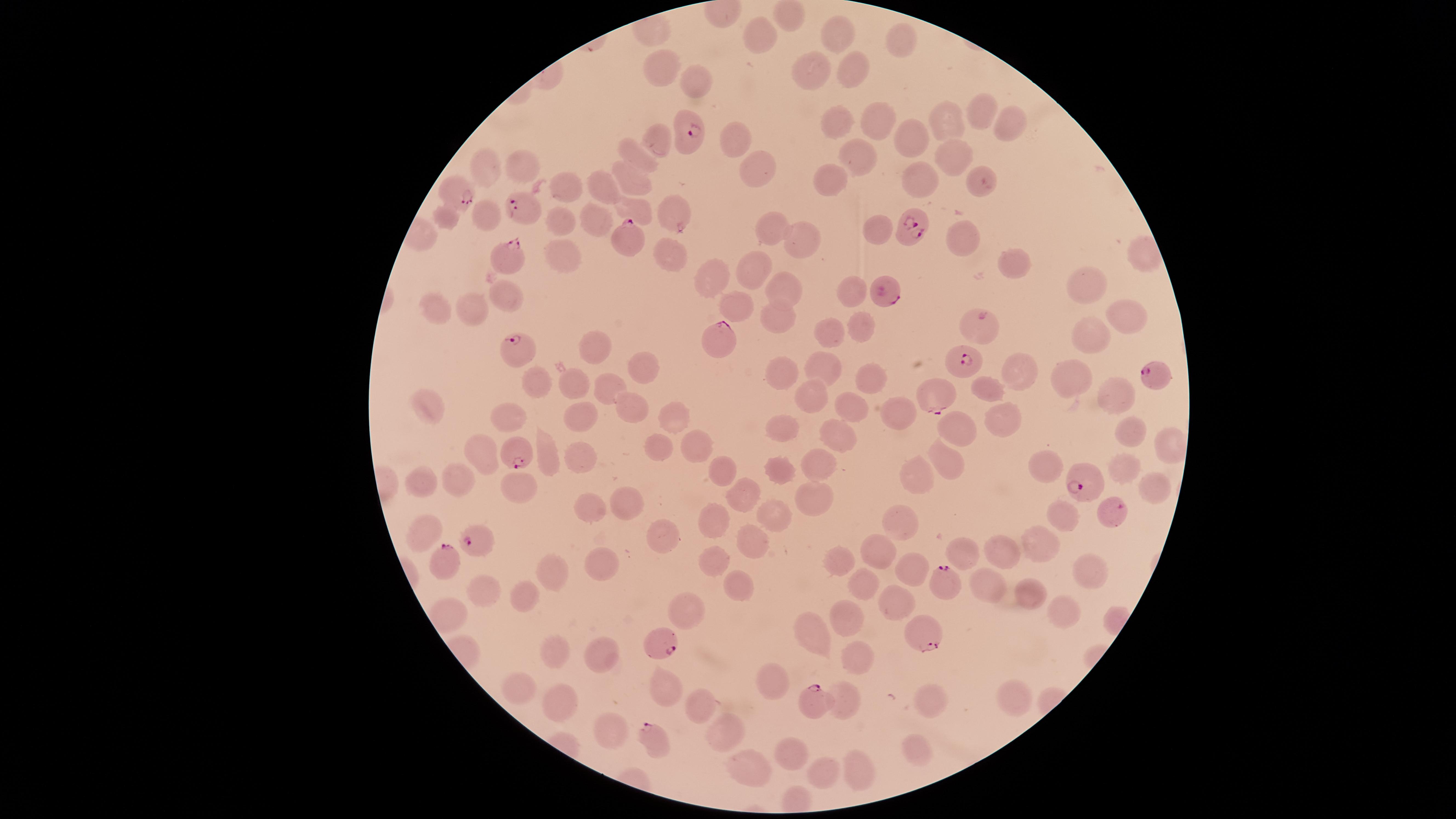
parasitized_RBCs: 'approximate marker points as [x, y] in pixels: [685, 136], [451, 189], [524, 211], [906, 226], [631, 241], [505, 253], [882, 292], [716, 340], [512, 354], [956, 361], [1156, 372], [934, 388], [514, 453], [1086, 478], [1110, 511], [481, 540], [443, 565], [946, 582], [921, 635], [660, 638], [813, 706], [650, 739]'
preparation: thin blood film
stain: Giemsa
field_of_view: single
uninfected_RBCs: 'approximate marker points as [x, y] in pixels: [840, 33], [765, 37], [905, 37], [856, 70], [658, 73], [819, 74], [695, 83], [982, 114], [880, 118], [945, 121], [1010, 124], [834, 126], [659, 139], [734, 139], [913, 140], [953, 154], [638, 155], [860, 155], [520, 167], [483, 169], [759, 172], [830, 178], [636, 181], [921, 182], [568, 183], [600, 191], [632, 207], [672, 212], [486, 214], [448, 218], [562, 219], [594, 219], [770, 226], [871, 229], [962, 241], [803, 242], [666, 255], [563, 259], [1014, 266], [754, 267], [711, 276], [850, 288], [507, 291], [783, 291], [1087, 291], [742, 306], [473, 310], [435, 312], [776, 315], [1126, 317], [865, 326], [835, 328], [978, 333], [1091, 336], [599, 353], [643, 366], [826, 367], [782, 374], [869, 375], [1027, 375], [1077, 380], [580, 383], [614, 384], [538, 386], [995, 390], [1113, 394], [816, 396], [430, 402], [634, 407], [854, 409], [899, 410], [580, 416], [674, 416], [1002, 419], [510, 420], [952, 429], [780, 430], [834, 432], [1129, 434], [693, 447], [658, 449], [488, 451], [547, 459], [579, 461], [813, 462], [943, 462], [1123, 463], [1046, 465], [724, 470], [778, 471], [917, 473], [456, 479], [425, 482], [1148, 488], [515, 492], [741, 492], [626, 498], [814, 500], [587, 508], [1059, 514], [778, 515], [717, 522], [899, 522], [421, 530], [660, 531], [1040, 537], [751, 540], [878, 551], [1004, 552], [969, 556], [594, 560], [717, 561], [840, 562], [912, 568], [553, 572], [1089, 575], [738, 585], [866, 586], [989, 588], [487, 589], [1031, 590], [526, 599], [891, 604], [687, 609], [1054, 612], [851, 616], [813, 630], [556, 650], [600, 652], [860, 653], [770, 680], [664, 686], [515, 687], [1010, 694], [844, 695], [934, 695], [562, 699], [700, 702], [612, 727], [724, 737], [914, 745], [793, 751], [857, 765], [747, 768], [823, 772]'
capture: smartphone photograph through the microscope eyepiece
visible_region: circular
species: Plasmodium falciparum
presence: malaria parasites detected
image_size: 1456×819 pixels